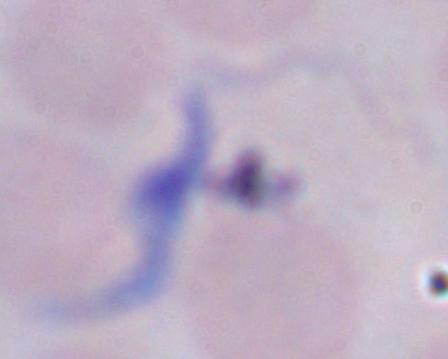

magnification = 1000x
identification = trypanosome
modality = micrograph